State the blood parasite species.
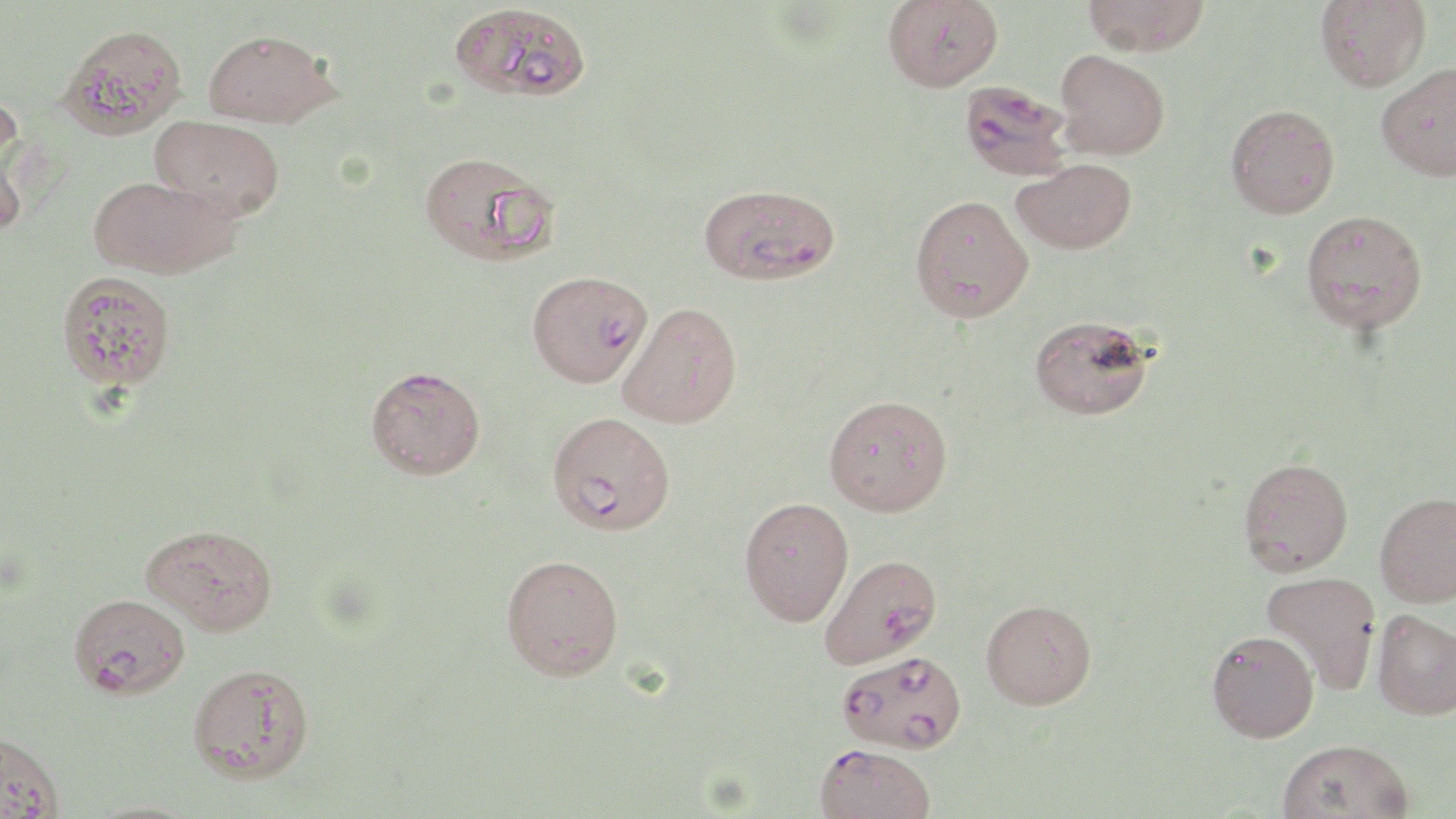

Plasmodium falciparum.

field of view = single
image size = 1456×819 pixels
modality = optical microscopy
uninfected red blood cell locations = approximate bounding boxes as named x1/y1/x2/y2 corners in pixels: (x1=883, y1=0, x2=1003, y2=91), (x1=1082, y1=0, x2=1211, y2=56), (x1=1316, y1=0, x2=1431, y2=92), (x1=450, y1=2, x2=590, y2=103), (x1=58, y1=23, x2=189, y2=140), (x1=203, y1=29, x2=341, y2=128), (x1=1054, y1=50, x2=1170, y2=159), (x1=1377, y1=62, x2=1456, y2=181), (x1=0, y1=84, x2=25, y2=196), (x1=1225, y1=104, x2=1340, y2=218), (x1=151, y1=115, x2=285, y2=221), (x1=0, y1=137, x2=30, y2=237), (x1=419, y1=150, x2=558, y2=265), (x1=1012, y1=158, x2=1136, y2=254), (x1=89, y1=175, x2=237, y2=279), (x1=909, y1=193, x2=1034, y2=322), (x1=1301, y1=209, x2=1427, y2=333), (x1=57, y1=270, x2=177, y2=391), (x1=619, y1=301, x2=742, y2=428), (x1=1029, y1=314, x2=1155, y2=420), (x1=824, y1=394, x2=953, y2=516), (x1=1239, y1=457, x2=1354, y2=575), (x1=1375, y1=492, x2=1456, y2=607), (x1=739, y1=496, x2=854, y2=626), (x1=143, y1=527, x2=279, y2=639), (x1=501, y1=553, x2=624, y2=680), (x1=1261, y1=571, x2=1382, y2=693), (x1=70, y1=593, x2=191, y2=700), (x1=981, y1=598, x2=1097, y2=709), (x1=1372, y1=608, x2=1456, y2=720), (x1=1207, y1=630, x2=1319, y2=742), (x1=188, y1=662, x2=314, y2=783), (x1=0, y1=731, x2=63, y2=819), (x1=1277, y1=738, x2=1415, y2=819), (x1=82, y1=800, x2=202, y2=819)
Plasmodium falciparum-infected red blood cell locations = approximate bounding boxes as named x1/y1/x2/y2 corners in pixels: (x1=958, y1=80, x2=1074, y2=181), (x1=699, y1=183, x2=841, y2=286), (x1=527, y1=270, x2=651, y2=387), (x1=365, y1=365, x2=485, y2=479), (x1=548, y1=411, x2=675, y2=536), (x1=819, y1=554, x2=943, y2=668), (x1=837, y1=650, x2=967, y2=754), (x1=814, y1=743, x2=936, y2=819)
preparation = thin blood smear
stain = May-Grünwald-Giemsa
magnification = 1000x